Classify this cell by malaria status.
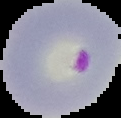
It is parasitized.

image type = cell region segmented out of the field of view; surrounding area masked to black
preparation = thin blood film
image size = 121×118 pixels